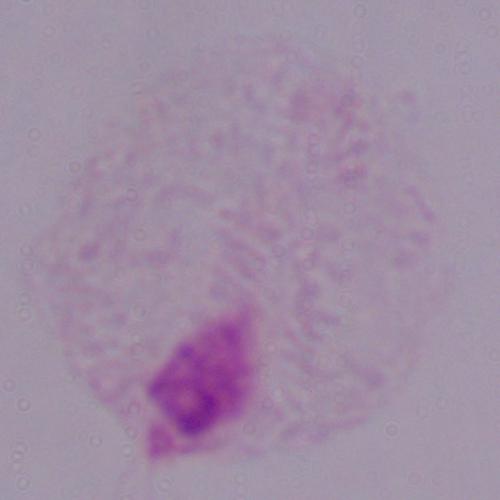

Captured at 1000x magnification. Photomicrograph. A trichomonad is shown.